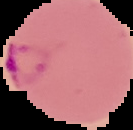
image type = segmented cell region with the area outside set to black
image size = 133×130 pixels
result = Plasmodium parasites detected
preparation = thin blood smear